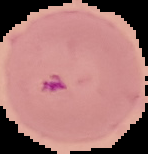

preparation: thin blood film
image_type: segmented cell region on a black background
malaria_status: parasitized
image_size: 148×154 pixels